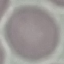

result = no malaria parasites detected
stain = Giemsa
capture = smartphone through the microscope eyepiece
preparation = thin blood smear
image type = automatically extracted cell patch, resized to 64 × 64 pixels